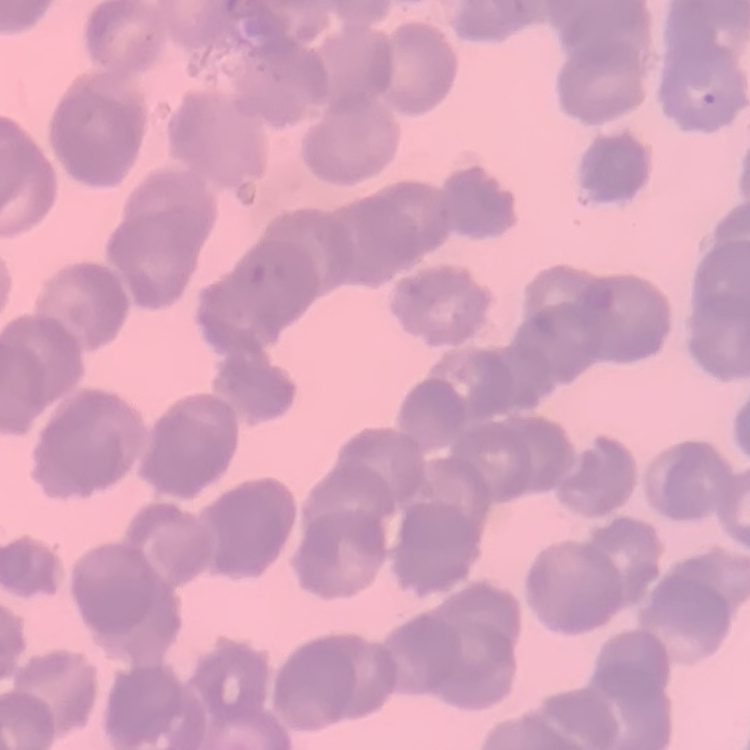
The erythrocytes exhibit rouleaux formation. Field's or Giemsa stain. One tile cut from a larger photomicrograph. Thin blood smear.